Assess this cell for malaria.
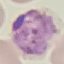
Parasitized.

Thin blood smear. Photographed with a smartphone camera at the microscope eyepiece. Automatically extracted cell patch, resized to 64 × 64 pixels. Giemsa-stained preparation.